Classify this cell by malaria status.
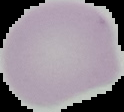

It is uninfected.

From a thin blood smear. The area outside the segmented cell region is set to black. Image is 124×112 pixels.